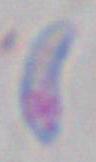
identification = Toxoplasma gondii
modality = micrograph
magnification = 1000x